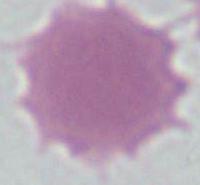

Micrograph. An erythrocyte is shown. 1000x magnification.